Report the malaria status of this cell.
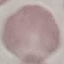

It is uninfected.

Acquired by smartphone through the microscope eyepiece. Thin smear of blood. Giemsa stain. Cell patch, automatically extracted from a larger field of view and resized to 64 × 64 pixels.